Name the cell type shown.
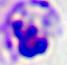

This is a leukocyte.

Micrograph. Captured at 400x magnification.